Describe the morphology of the red blood cells.
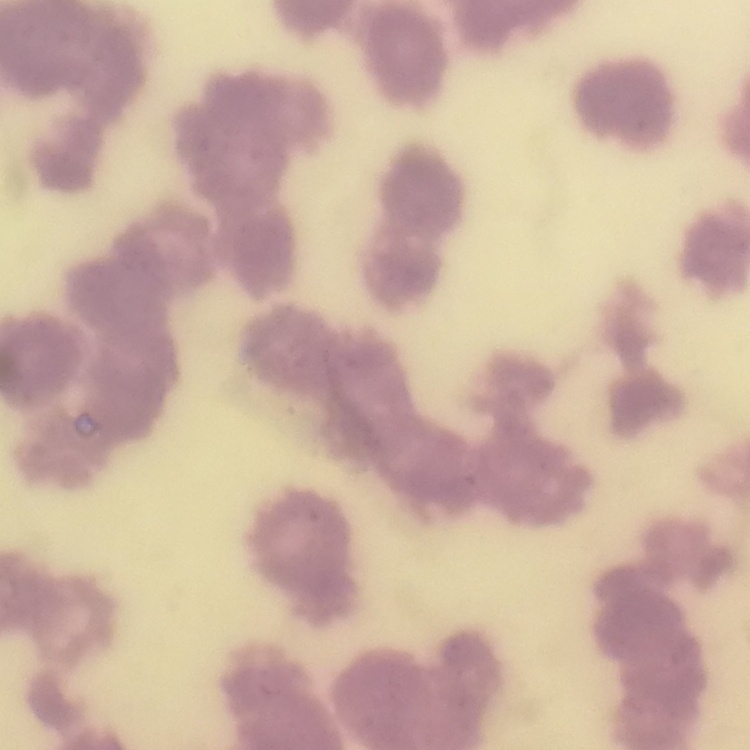

Rouleaux formation.

Summary:
  - Image type: square crop of a larger photomicrograph
  - Preparation: thin blood film
  - Stain: Field's or Giemsa